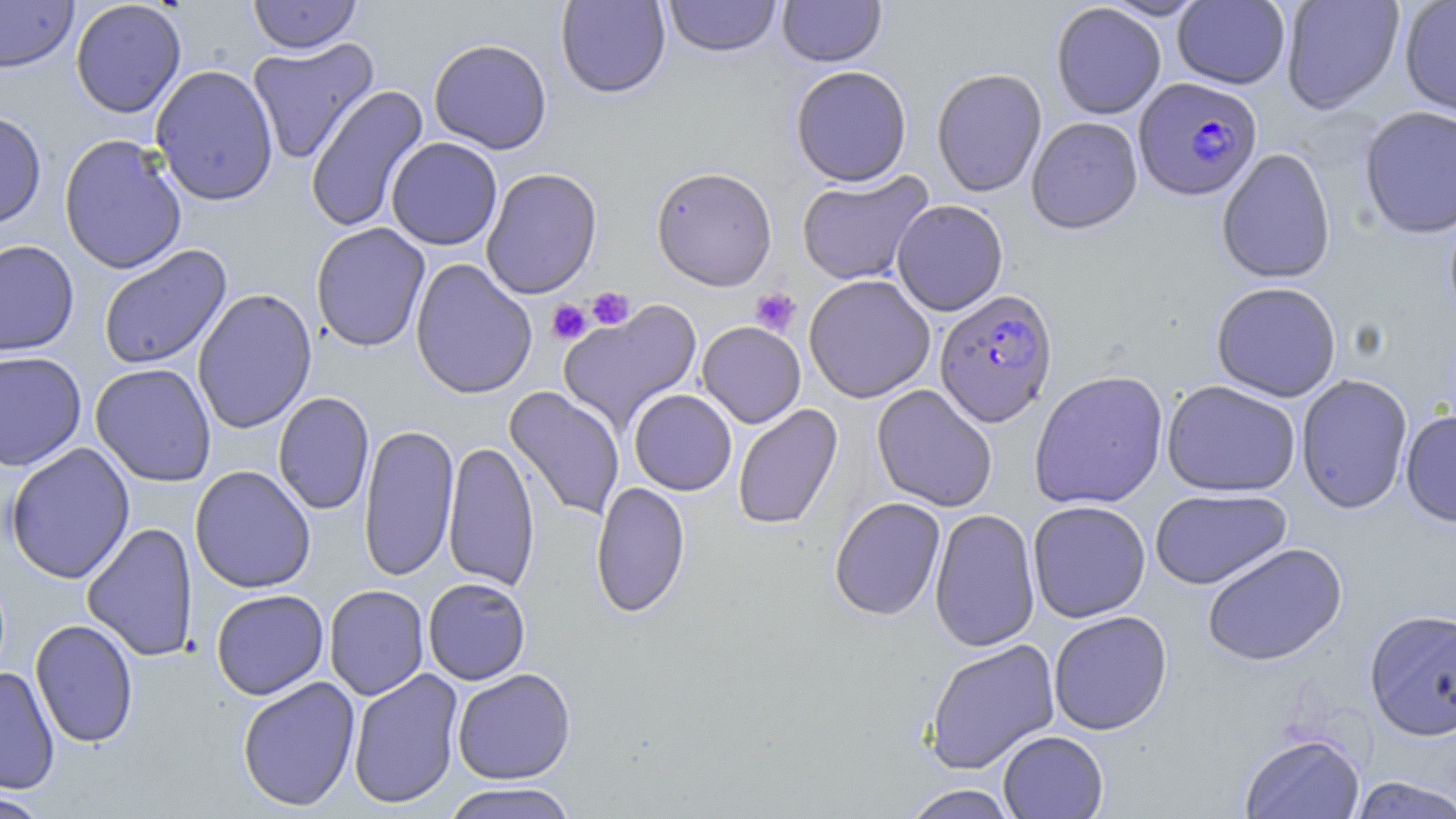
Approximate bounding boxes as (x1,y1)-(x2,y2) corner pairs in pixels. Uninfected red blood cell locations: (0,0)-(78,73), (70,0)-(187,118), (248,0)-(362,54), (555,0)-(671,98), (663,0)-(781,57), (777,0)-(887,67), (1099,0)-(1210,21), (1281,0)-(1404,113), (1399,0)-(1456,117), (1173,1)-(1291,88), (1051,3)-(1166,119), (247,37)-(379,165), (428,38)-(553,154), (150,64)-(279,206), (790,65)-(912,186), (931,67)-(1047,197), (305,85)-(430,233), (1359,105)-(1456,239), (0,110)-(47,230), (1026,116)-(1142,234), (58,133)-(188,275), (386,137)-(502,250), (1217,147)-(1336,284), (651,166)-(778,291), (481,167)-(602,299), (797,170)-(934,286), (891,199)-(1008,316), (310,222)-(431,352), (0,239)-(80,356), (98,245)-(232,371), (410,258)-(538,400), (804,274)-(935,403), (1211,281)-(1342,402), (192,288)-(317,434), (558,300)-(702,432), (696,321)-(806,428), (0,350)-(87,471), (90,363)-(216,487), (1029,369)-(1169,510), (1296,374)-(1413,514), (1161,380)-(1300,497), (871,384)-(998,512), (504,386)-(625,521), (629,389)-(737,495), (273,392)-(374,515), (733,404)-(842,530), (1401,410)-(1456,527), (359,422)-(458,583), (443,439)-(540,592), (3,442)-(136,584), (190,465)-(316,593), (590,481)-(691,618), (1149,488)-(1291,590), (829,497)-(946,621), (1028,500)-(1151,622), (929,508)-(1041,652), (82,521)-(199,662), (1202,542)-(1347,666), (423,577)-(531,685), (324,585)-(429,701), (211,589)-(329,699), (1364,608)-(1456,739), (1048,610)-(1173,735), (30,619)-(139,748), (923,638)-(1060,774), (0,667)-(60,795), (347,668)-(464,809), (452,668)-(576,784), (237,676)-(361,811), (998,730)-(1108,819), (1239,732)-(1365,819), (1347,777)-(1456,818), (438,782)-(581,819), (901,784)-(1020,818), (0,791)-(52,818). Platelet locations: (749,287)-(801,337), (587,288)-(635,330), (546,299)-(592,345). Plasmodium falciparum-infected red blood cell locations: (1134,77)-(1261,200), (934,289)-(1057,427). Slide-level diagnosis: Plasmodium falciparum. Single field of view. Thin blood smear. May-Grünwald-Giemsa-stained preparation. Captured at 1000x magnification. Image is 1456×819 pixels. Light microscopy.